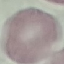
Malaria status: uninfected. Thin smear of blood. Giemsa stain. Acquired by smartphone through the microscope eyepiece. Automatically extracted cell patch, resized to 64 × 64 pixels.